Classify this cell by malaria status.
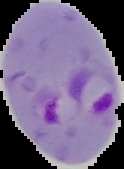
Parasitized.

Image is 124×169 pixels. Cell region segmented out of the field of view; the surrounding area is masked to black. From a thin blood film.